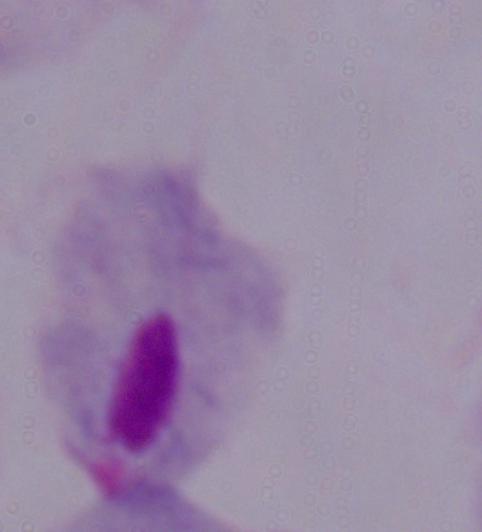
magnification = 1000x
modality = micrograph
identification = trichomonad